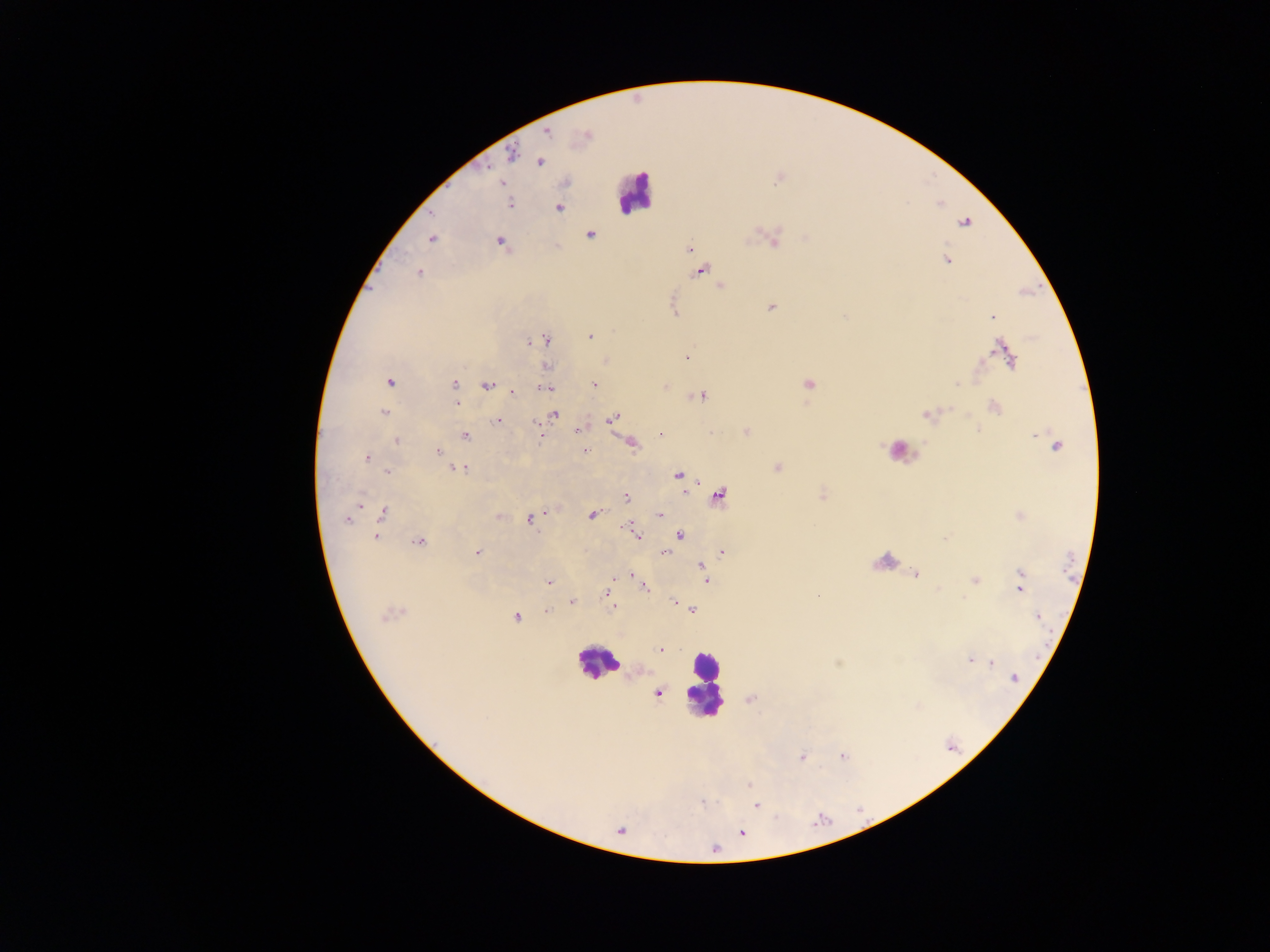

leukocyte_locations: 'approximate centers as (x, y) in pixels: (634, 192), (897, 448), (882, 560), (598, 661), (704, 685)'
image_size: 1270×952 pixels
capture: mobile-phone photograph through a microscope
preparation: thick blood smear
plasmodium_parasite_locations: 'approximate centers as (x, y) in pixels: (546, 132), (585, 136), (511, 154), (540, 162), (779, 178), (501, 183), (510, 204), (558, 208), (964, 221), (590, 234), (431, 238), (774, 240), (500, 241), (688, 249), (947, 260), (701, 270), (418, 273), (719, 286), (771, 307), (674, 312), (992, 317), (590, 336), (545, 339), (529, 342), (1000, 349), (686, 357), (1010, 360), (606, 361), (547, 367), (389, 382), (454, 384), (593, 384), (807, 384), (487, 385), (664, 386), (547, 388), (512, 392), (701, 394), (456, 402), (994, 407), (383, 412), (928, 413), (554, 415), (612, 418), (498, 421), (579, 429), (977, 430), (746, 431), (662, 433), (465, 435), (397, 440), (631, 442), (1057, 445), (584, 450), (438, 452), (366, 457), (458, 468), (777, 468), (385, 471), (678, 474), (822, 494), (719, 495), (626, 497), (359, 505), (547, 511), (383, 512), (592, 514), (659, 515), (499, 516), (1020, 516), (530, 518), (346, 519), (628, 527), (635, 533), (679, 535), (375, 536), (945, 538), (419, 542), (477, 552), (664, 552), (721, 552), (703, 567), (706, 572), (1020, 573), (630, 575), (916, 575), (974, 580), (706, 581), (549, 582), (644, 587), (1019, 588), (607, 592), (673, 600), (572, 601), (613, 608), (693, 609), (547, 611), (390, 613), (1037, 615), (516, 617), (660, 649), (970, 659), (991, 662), (1013, 677), (657, 693), (749, 699), (842, 755), (802, 756), (756, 805), (619, 829)'
country: Ghana
field_of_view: single